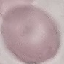

{
  "malaria_status": "uninfected",
  "image_type": "cell patch, automatically extracted from a larger field of view and resized to 64 × 64 pixels",
  "capture": "smartphone through the microscope eyepiece",
  "stain": "Giemsa",
  "preparation": "thin blood smear"
}